Name the parasite shown.
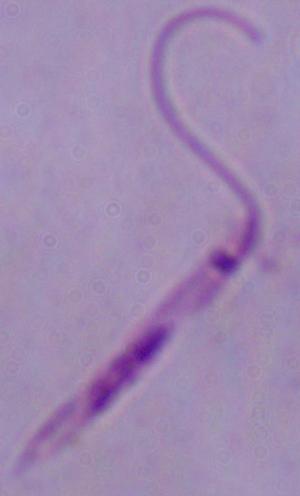

This is Leishmania.

Photomicrograph. Captured at 1000x magnification.